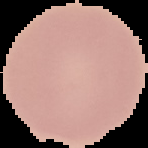 From a thin blood film. The area outside the segmented cell region is set to black. Result: no Plasmodium parasites detected. Image is 148×148 pixels.